Comment on the morphology of the red blood cells.
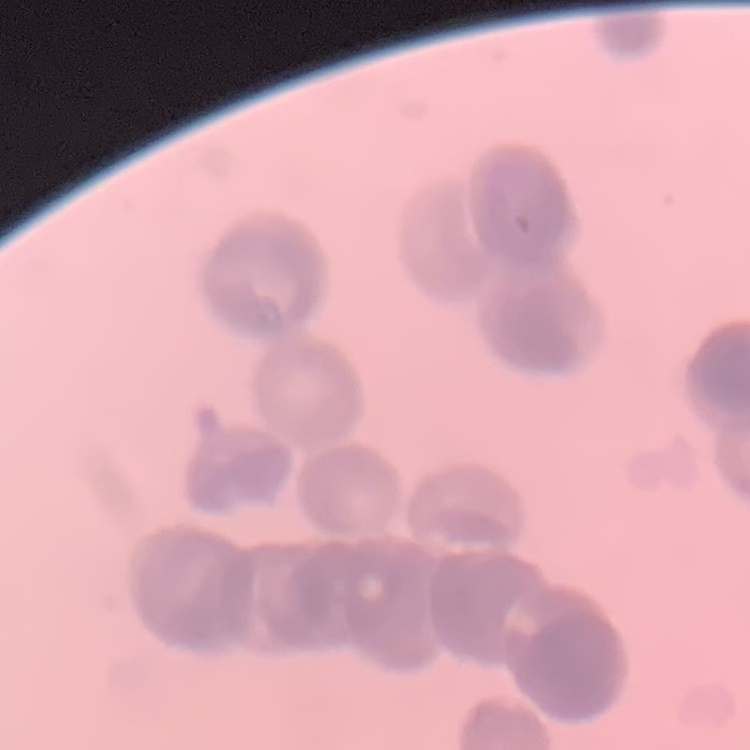
Rouleaux formation.

Summary:
  - Stain: Field's or Giemsa
  - Preparation: thin blood smear
  - Image type: square crop of a larger photomicrograph